Assess for malaria.
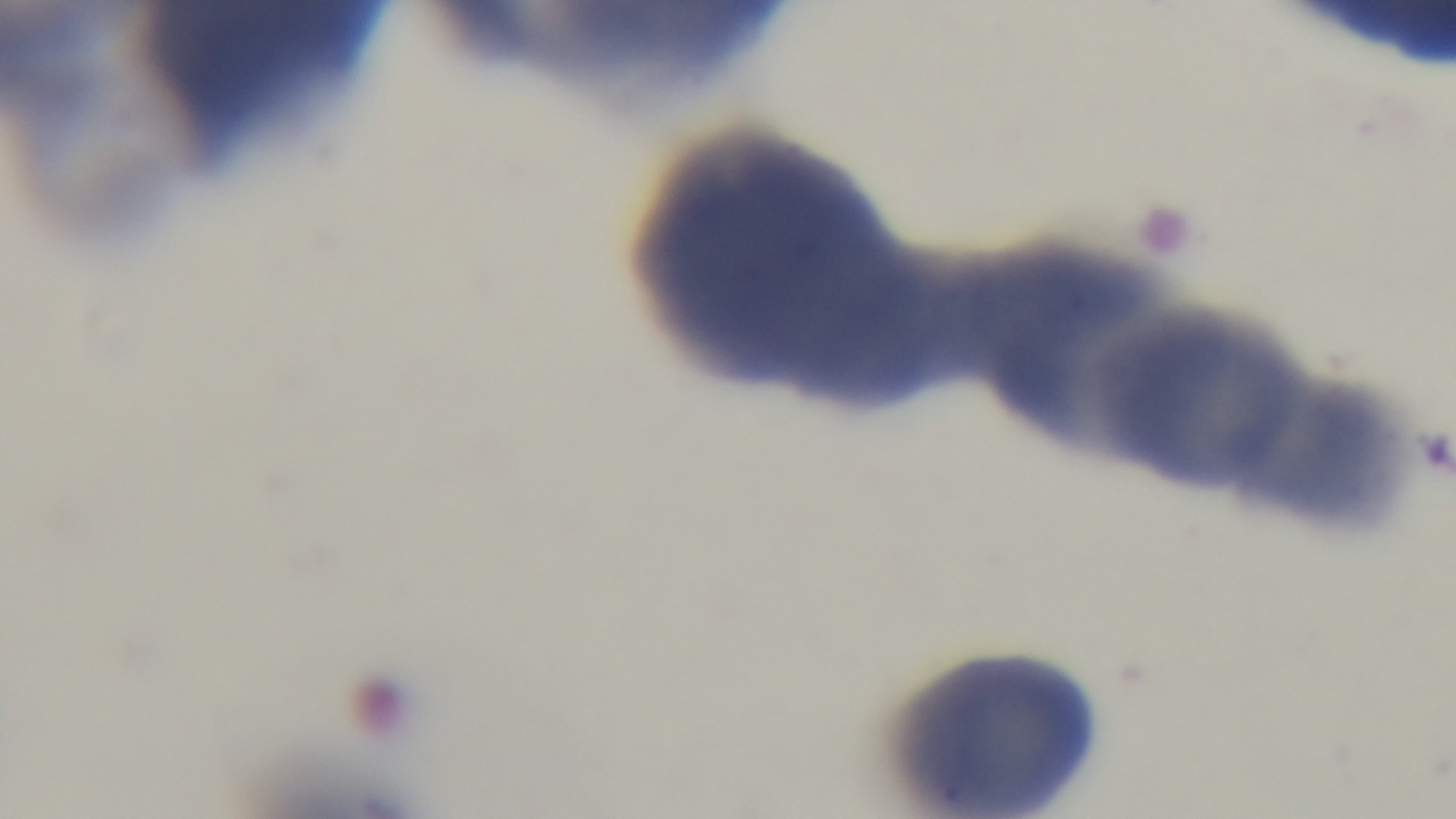
Uninfected.

{
  "modality": "light microscopy",
  "field_of_view": "single",
  "stain": "Giemsa",
  "preparation": "thin blood film",
  "capture": "mounted 4K digital camera",
  "objective": "100x oil immersion"
}